Name the parasite shown.
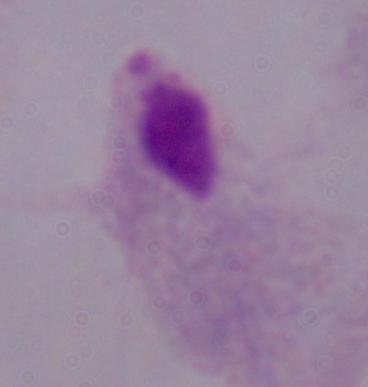

This is a trichomonad.

Summary:
  - Magnification: 1000x
  - Modality: micrograph